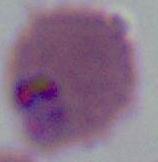

Photomicrograph. 400x or 1000x magnification. A Plasmodium parasite is shown.